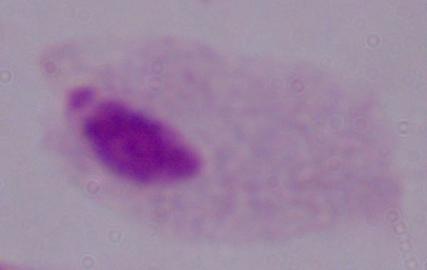

magnification = 1000x
modality = micrograph
identification = trichomonad